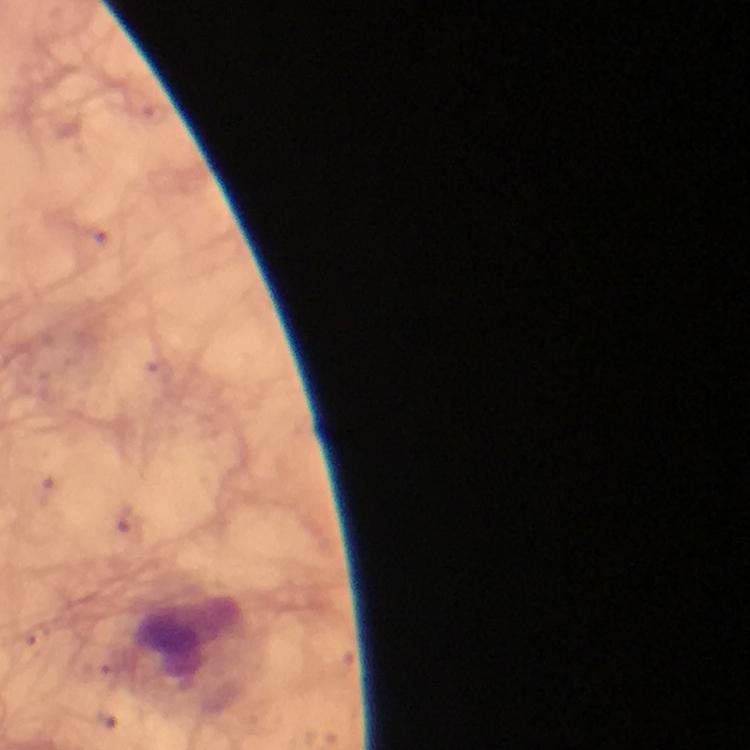 Approximate object centers, in pixels from the top-left corner. Leukocyte locations: (x=195, y=644). Giemsa-stained preparation. At 100x magnification. Cropped region of a single field of view. Plasmodium parasites: none detected. Smartphone photograph taken through a microscope. Thick smear. Image is 750×750 pixels. Immersion oil applied. From a malaria diagnostic workup.